Name the parasite shown.
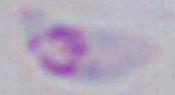
Toxoplasma gondii.

{
  "modality": "photomicrograph",
  "magnification": "1000x"
}